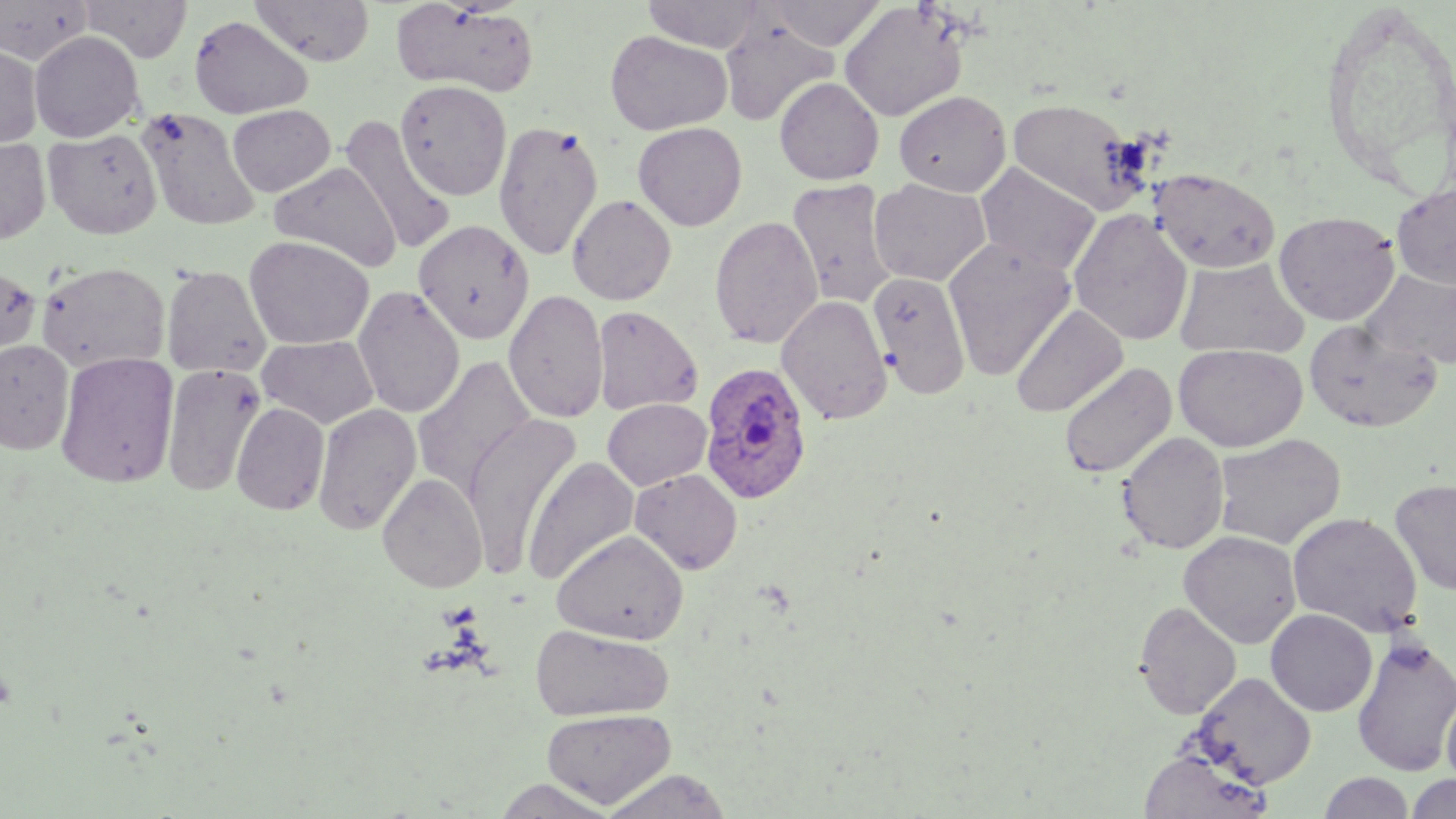
Plasmodium ovale-infected red blood cell locations = approximate bounding boxes as named x1/y1/x2/y2 corners in pixels: (x1=700, y1=361, x2=813, y2=504)
slide-level diagnosis = Plasmodium ovale
image size = 1456×819 pixels
field of view = one of a larger specimen
modality = optical microscopy
magnification = 1000x
stain = May-Grünwald-Giemsa
uninfected red blood cell locations = approximate bounding boxes as named x1/y1/x2/y2 corners in pixels: (x1=79, y1=0, x2=192, y2=62), (x1=251, y1=0, x2=375, y2=66), (x1=641, y1=0, x2=768, y2=52), (x1=764, y1=0, x2=886, y2=51), (x1=0, y1=1, x2=93, y2=64), (x1=391, y1=2, x2=541, y2=97), (x1=838, y1=2, x2=967, y2=122), (x1=188, y1=14, x2=313, y2=119), (x1=719, y1=19, x2=838, y2=126), (x1=605, y1=30, x2=732, y2=135), (x1=29, y1=31, x2=144, y2=142), (x1=0, y1=43, x2=42, y2=150), (x1=774, y1=77, x2=884, y2=185), (x1=395, y1=79, x2=512, y2=201), (x1=894, y1=90, x2=1011, y2=196), (x1=1007, y1=97, x2=1146, y2=214), (x1=227, y1=104, x2=336, y2=196), (x1=137, y1=108, x2=262, y2=231), (x1=339, y1=118, x2=457, y2=256), (x1=494, y1=120, x2=604, y2=261), (x1=632, y1=122, x2=747, y2=231), (x1=43, y1=127, x2=162, y2=239), (x1=0, y1=137, x2=52, y2=245), (x1=270, y1=161, x2=402, y2=272), (x1=976, y1=163, x2=1101, y2=276), (x1=1149, y1=167, x2=1281, y2=273), (x1=869, y1=178, x2=990, y2=287), (x1=787, y1=179, x2=899, y2=309), (x1=1391, y1=184, x2=1456, y2=289), (x1=567, y1=194, x2=677, y2=305), (x1=1068, y1=208, x2=1193, y2=347), (x1=1274, y1=210, x2=1401, y2=326), (x1=709, y1=215, x2=822, y2=349), (x1=412, y1=219, x2=534, y2=344), (x1=244, y1=235, x2=374, y2=350), (x1=944, y1=238, x2=1076, y2=380), (x1=1175, y1=256, x2=1309, y2=359), (x1=36, y1=261, x2=170, y2=373), (x1=0, y1=264, x2=42, y2=363), (x1=161, y1=265, x2=272, y2=379), (x1=1363, y1=268, x2=1456, y2=370), (x1=869, y1=271, x2=970, y2=400), (x1=353, y1=285, x2=466, y2=418), (x1=503, y1=289, x2=609, y2=424), (x1=777, y1=294, x2=892, y2=425), (x1=1011, y1=303, x2=1127, y2=418), (x1=592, y1=305, x2=703, y2=416), (x1=1303, y1=318, x2=1444, y2=433), (x1=257, y1=335, x2=379, y2=429), (x1=0, y1=340, x2=74, y2=455), (x1=1173, y1=343, x2=1307, y2=451), (x1=55, y1=352, x2=179, y2=489), (x1=413, y1=355, x2=537, y2=498), (x1=1058, y1=362, x2=1177, y2=479), (x1=161, y1=363, x2=265, y2=497), (x1=602, y1=398, x2=712, y2=490), (x1=231, y1=402, x2=330, y2=515), (x1=312, y1=403, x2=422, y2=535), (x1=463, y1=414, x2=581, y2=574), (x1=1117, y1=432, x2=1229, y2=554), (x1=1213, y1=433, x2=1346, y2=549), (x1=522, y1=456, x2=640, y2=586), (x1=629, y1=468, x2=743, y2=574), (x1=377, y1=473, x2=487, y2=592), (x1=1389, y1=478, x2=1456, y2=595), (x1=1287, y1=511, x2=1423, y2=637), (x1=551, y1=529, x2=689, y2=645), (x1=1179, y1=530, x2=1302, y2=648), (x1=1133, y1=600, x2=1241, y2=719), (x1=1266, y1=608, x2=1377, y2=716), (x1=529, y1=624, x2=675, y2=721), (x1=1352, y1=634, x2=1456, y2=777), (x1=1192, y1=671, x2=1317, y2=789), (x1=1441, y1=689, x2=1456, y2=792), (x1=541, y1=707, x2=676, y2=808), (x1=1138, y1=746, x2=1271, y2=819), (x1=600, y1=769, x2=733, y2=819), (x1=1319, y1=772, x2=1414, y2=818), (x1=1405, y1=773, x2=1456, y2=819), (x1=489, y1=777, x2=620, y2=817)
preparation = thin blood film